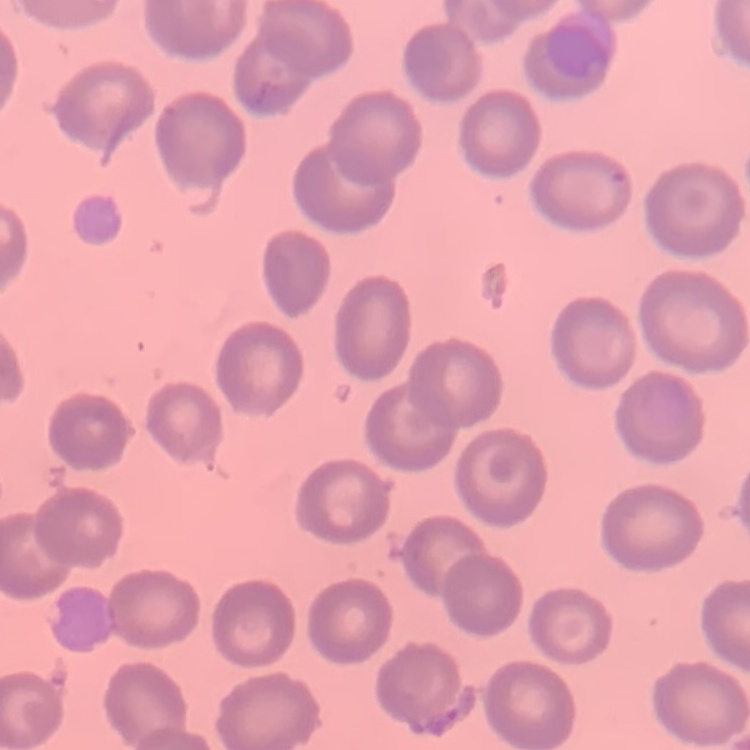

The erythrocytes show no rouleaux formation. Field's or Giemsa stain. Thin blood film. One tile cut from a larger photomicrograph.